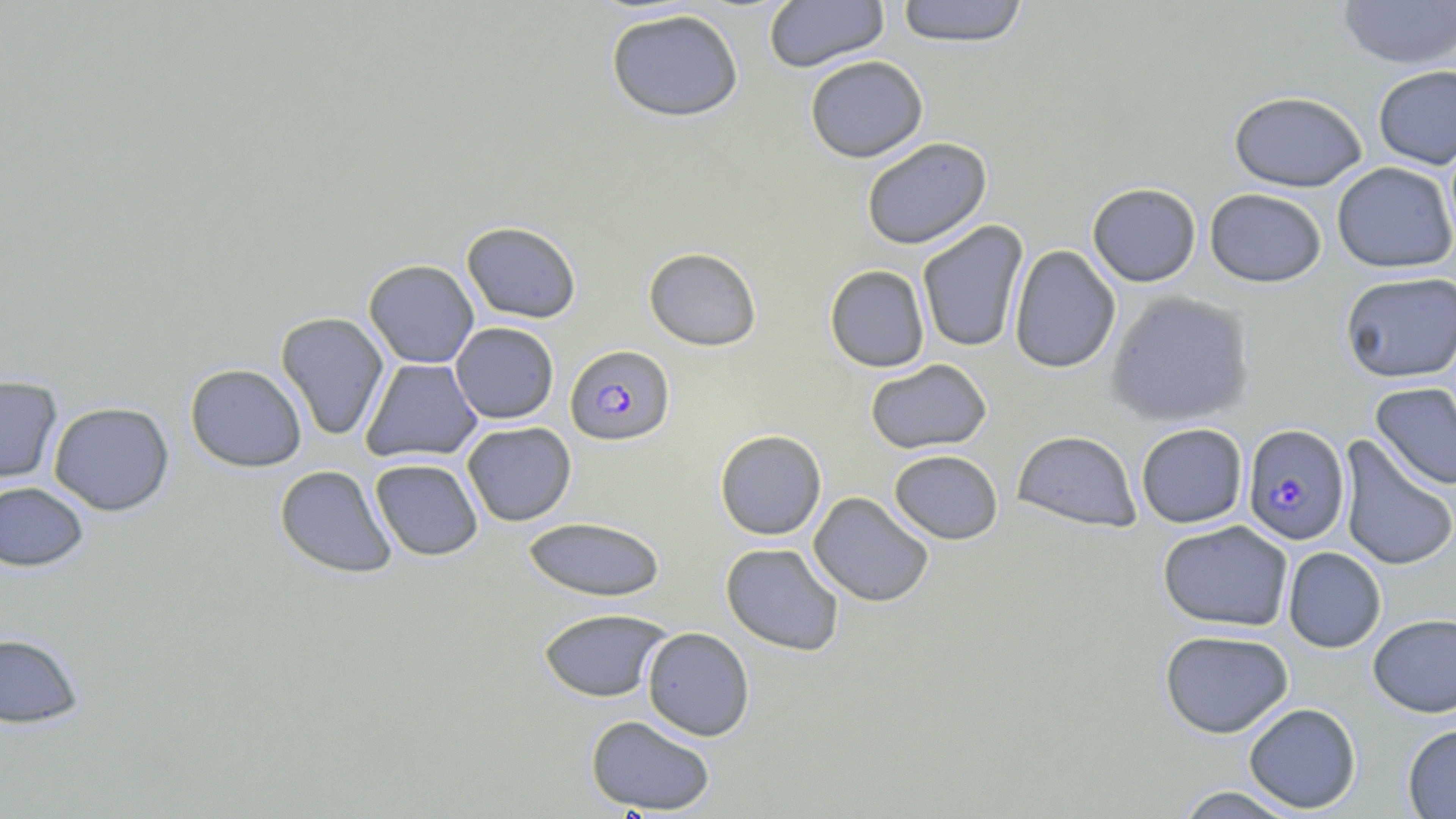
{
  "slide_level_diagnosis": "Plasmodium falciparum",
  "magnification": "1000x",
  "plasmodium_falciparum_infected_red_blood_cell_locations": "approximate bounding boxes as (x1,y1)-(x2,y2) corner pairs in pixels: (566,344)-(675,445), (1242,423)-(1350,545)",
  "image_size": "1456×819 pixels",
  "uninfected_red_blood_cell_locations": "approximate bounding boxes as (x1,y1)-(x2,y2) corner pairs in pixels: (764,0)-(889,73), (895,0)-(1030,47), (1337,0)-(1456,69), (605,9)-(744,123), (805,55)-(928,162), (1373,64)-(1456,170), (1228,90)-(1368,192), (861,136)-(992,250), (1332,162)-(1456,274), (1087,182)-(1201,287), (1204,188)-(1327,288), (917,220)-(1029,354), (461,221)-(581,323), (1008,245)-(1121,374), (643,247)-(762,351), (363,259)-(479,368), (824,264)-(930,372), (1340,271)-(1456,383), (1104,290)-(1255,428), (276,311)-(389,441), (450,322)-(558,423), (360,358)-(483,463), (864,358)-(992,455), (184,363)-(307,472), (0,375)-(62,484), (1370,382)-(1456,492), (48,401)-(174,516), (462,422)-(576,526), (1136,423)-(1248,528), (714,429)-(827,540), (1012,430)-(1142,532), (1337,436)-(1456,571), (889,449)-(1003,544), (370,458)-(483,560), (274,465)-(397,578), (0,481)-(88,571), (808,492)-(934,607), (523,516)-(665,602), (1157,520)-(1293,633), (720,543)-(845,657), (1282,547)-(1386,653), (537,608)-(671,702), (1368,613)-(1456,717), (642,627)-(755,741), (1159,629)-(1294,738), (0,633)-(84,728), (1243,702)-(1362,813), (585,714)-(716,815), (1402,724)-(1456,818), (1173,785)-(1303,818)",
  "modality": "light microscopy",
  "stain": "May-Grünwald-Giemsa",
  "field_of_view": "single",
  "preparation": "thin blood smear"
}